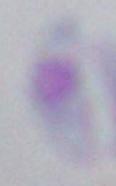
Summary:
  - Identification: Toxoplasma gondii
  - Modality: photomicrograph
  - Magnification: 1000x